Classify this cell by malaria status.
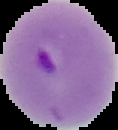

It is parasitized.

Summary:
  - Image size: 118×130 pixels
  - Preparation: thin blood film
  - Image type: segmented cell region on a black background